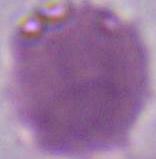
identification = red blood cell
modality = photomicrograph
magnification = 1000x